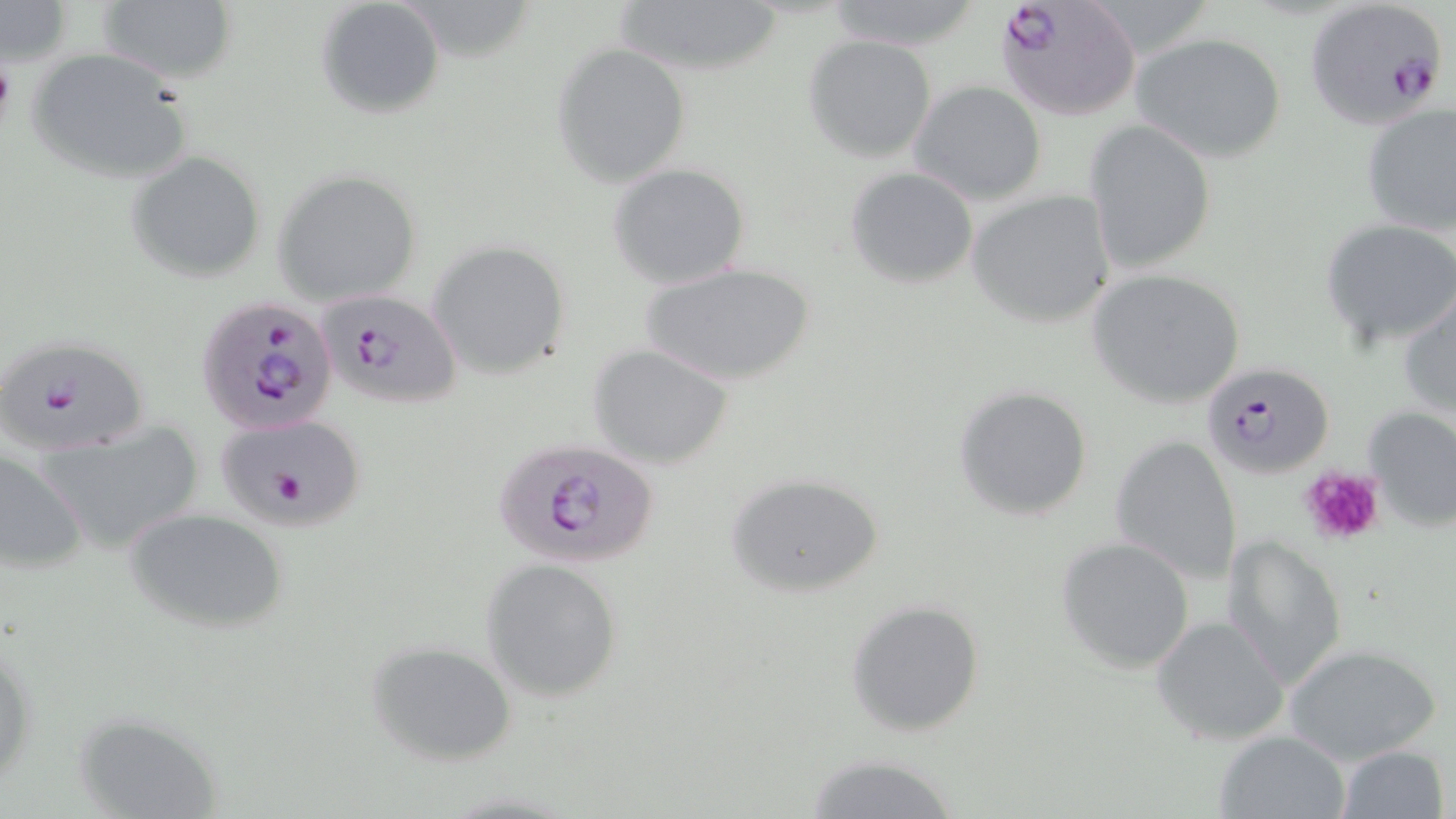
slide_level_diagnosis: Plasmodium falciparum
preparation: thin blood film
field_of_view: single
plasmodium_falciparum_infected_red_blood_cell_locations: 'approximate bounding boxes as [x1, y1, x2, y2] in pixels: [995, 1, 1140, 122], [1304, 1, 1450, 129], [313, 288, 464, 411], [196, 297, 340, 435], [2, 334, 152, 456], [1203, 361, 1332, 480], [215, 412, 367, 532], [492, 440, 660, 572]'
modality: optical microscopy
magnification: 1000x
stain: May-Grünwald-Giemsa
uninfected_red_blood_cell_locations: 'approximate bounding boxes as [x1, y1, x2, y2] in pixels: [609, 0, 790, 77], [97, 1, 238, 85], [315, 1, 445, 120], [819, 1, 987, 51], [1, 2, 73, 67], [1131, 30, 1288, 163], [803, 36, 937, 161], [553, 43, 690, 186], [26, 49, 193, 184], [910, 80, 1046, 205], [1360, 102, 1455, 236], [1083, 119, 1216, 276], [127, 151, 267, 282], [609, 164, 751, 289], [844, 166, 978, 289], [275, 169, 424, 306], [966, 190, 1116, 328], [1321, 218, 1456, 347], [427, 240, 572, 381], [639, 261, 818, 387], [1087, 268, 1249, 411], [1399, 288, 1456, 419], [588, 343, 736, 468], [952, 384, 1096, 522], [1363, 404, 1456, 530], [34, 423, 205, 554], [1111, 434, 1243, 585], [0, 448, 87, 575], [724, 470, 887, 598], [124, 507, 288, 635], [1222, 532, 1351, 687], [1056, 537, 1195, 672], [481, 557, 625, 701], [844, 599, 987, 737], [1152, 617, 1289, 745], [1, 621, 37, 794], [366, 639, 520, 766], [1283, 643, 1443, 765], [1214, 729, 1352, 819], [1336, 744, 1449, 819], [803, 755, 967, 818]'
platelet_locations: 'approximate bounding boxes as [x1, y1, x2, y2] in pixels: [0, 56, 15, 126], [1298, 466, 1387, 548]'
image_size: 1456×819 pixels